Name the parasite shown.
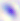

Toxoplasma gondii.

magnification = 400x
modality = micrograph